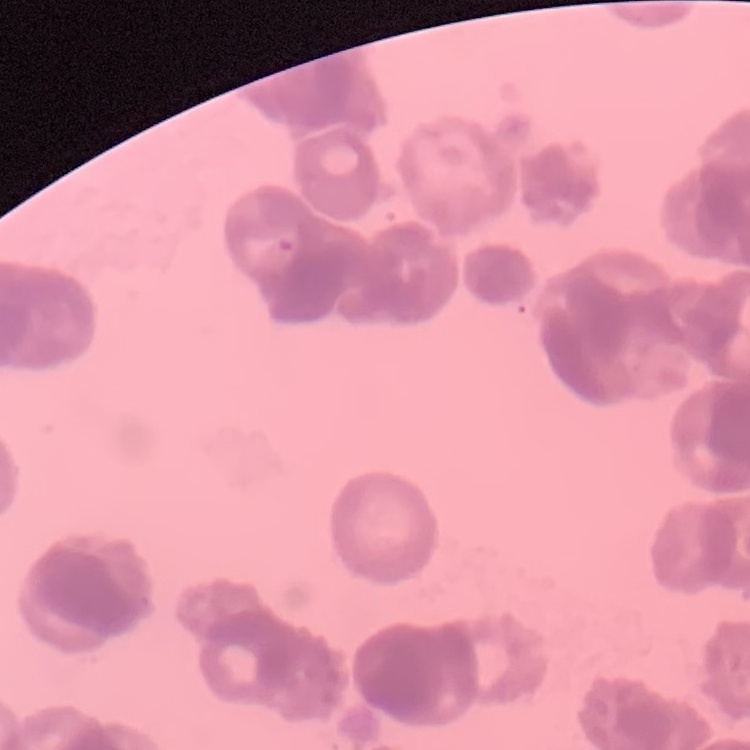
The red blood cells show rouleaux formation. Stained with either Field's or Giemsa. Square crop of a larger photomicrograph. Thin blood film.